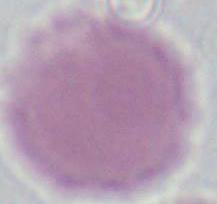

Summary:
  - Identification: red blood cell
  - Magnification: 1000x
  - Modality: photomicrograph